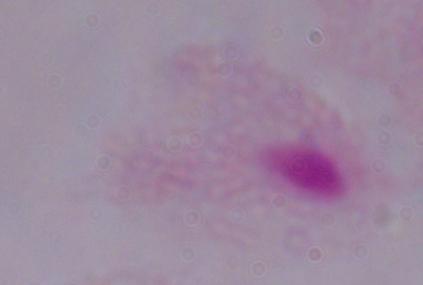

1000x magnification. A trichomonad is seen. Micrograph.